Report the malaria status of this cell.
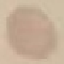
It is uninfected.

Summary:
  - Stain: Giemsa
  - Image type: cell patch, automatically extracted from a larger field of view and resized to 64 × 64 pixels
  - Preparation: thin blood smear
  - Capture: smartphone camera at the microscope eyepiece